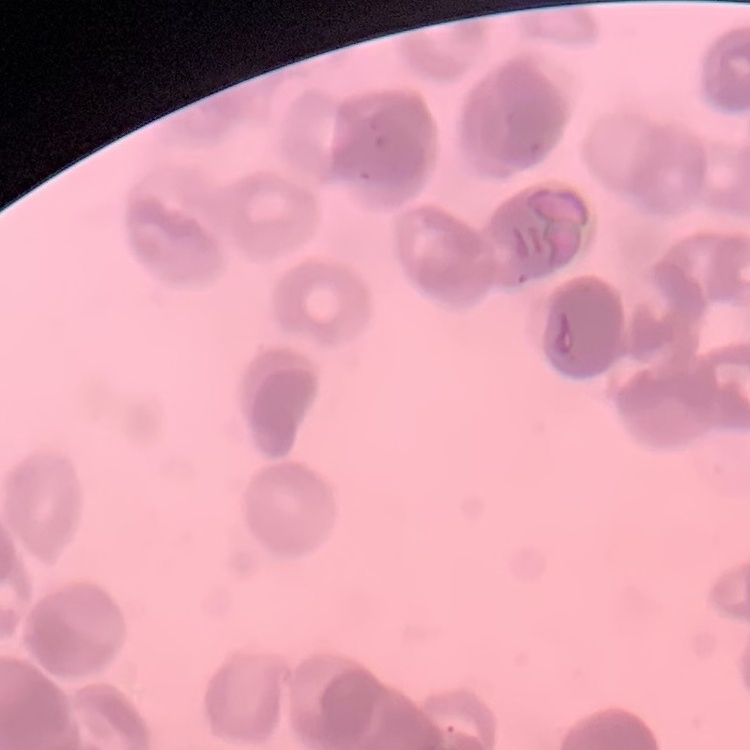

red blood cell morphology = rouleaux formation
stain = Field's or Giemsa
image type = square crop of a larger photomicrograph
preparation = thin blood film